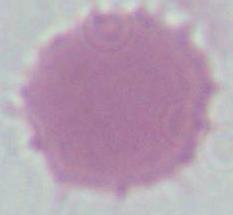
Summary:
  - Identification: erythrocyte
  - Magnification: 1000x
  - Modality: photomicrograph